Locate and identify every blood parasite.
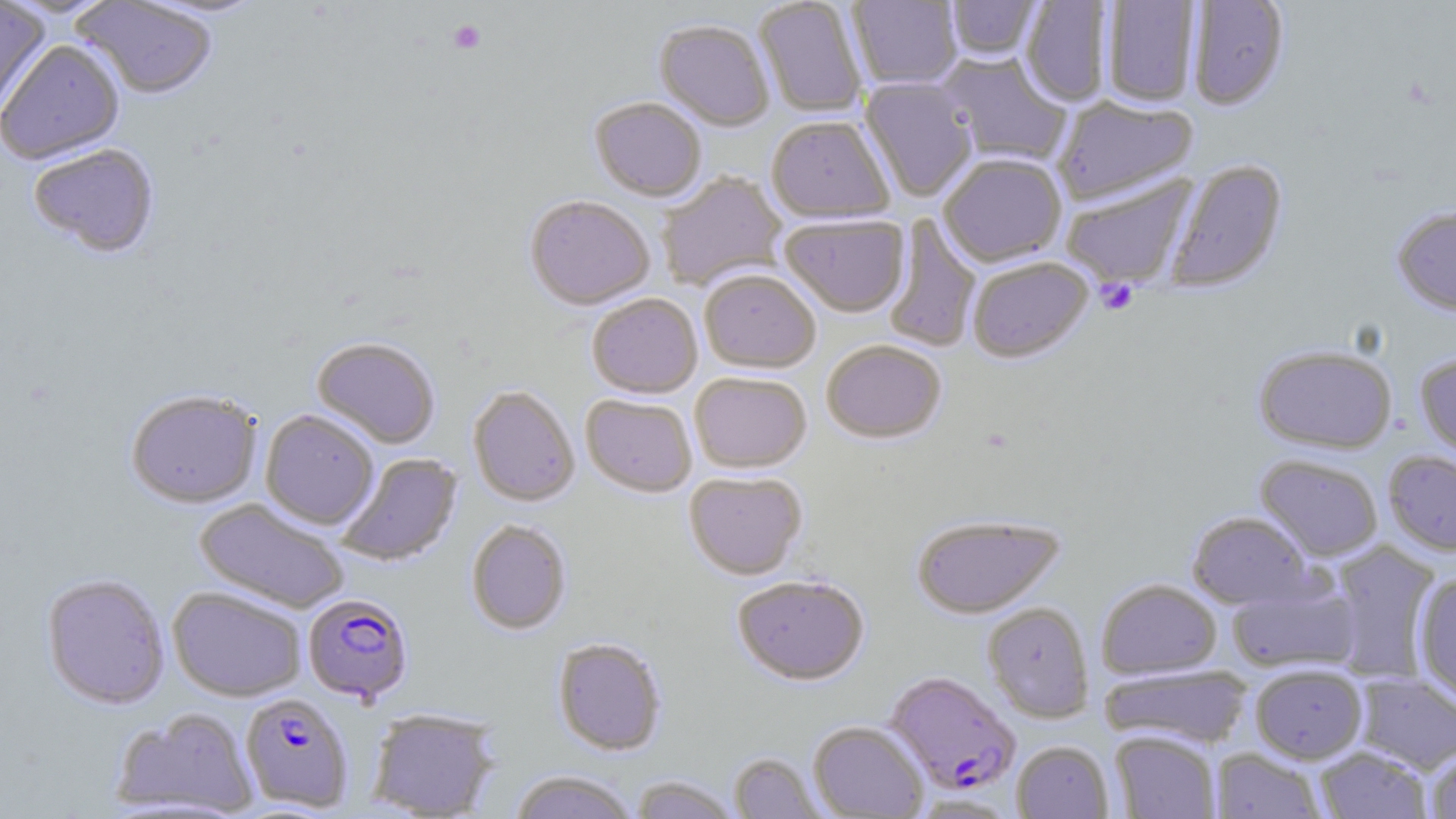

Approximate bounding boxes as (x1, y1, x2, y2) in pixels.
Plasmodium falciparum-infected red blood cells: (302, 593, 415, 704), (884, 670, 1021, 795), (240, 692, 354, 812).
No Plasmodium ovale, Plasmodium malariae, Plasmodium vivax, Babesia divergens, or Trypanosoma brucei observed.

{
  "slide_level_diagnosis": "Plasmodium falciparum",
  "image_size": "1456×819 pixels",
  "magnification": "1000x",
  "modality": "light microscopy",
  "uninfected_red_blood_cell_locations": "approximate bounding boxes as (x1, y1, x2, y2) in pixels: (753, 0, 868, 118), (847, 0, 962, 90), (1185, 0, 1290, 111), (0, 1, 51, 120), (71, 1, 218, 99), (945, 1, 1043, 63), (1020, 1, 1114, 107), (1101, 1, 1201, 106), (654, 20, 775, 131), (1, 40, 125, 165), (936, 52, 1072, 166), (859, 77, 978, 202), (1053, 95, 1198, 205), (590, 97, 706, 201), (766, 115, 895, 223), (27, 143, 159, 258), (938, 153, 1067, 267), (1165, 158, 1288, 294), (656, 172, 787, 291), (1060, 174, 1197, 289), (525, 194, 655, 310), (1391, 205, 1456, 316), (780, 214, 909, 317), (883, 216, 981, 354), (967, 255, 1093, 363), (699, 268, 821, 373), (587, 293, 702, 398), (312, 336, 440, 449), (323, 338, 448, 567), (821, 339, 946, 443), (1254, 344, 1397, 454), (1414, 352, 1456, 466), (689, 371, 812, 473), (467, 385, 580, 506), (125, 389, 262, 509), (581, 394, 697, 496), (260, 409, 379, 529), (1383, 450, 1456, 556), (336, 452, 462, 567), (1255, 454, 1383, 561), (684, 471, 808, 580), (195, 498, 350, 614), (1187, 511, 1313, 609), (911, 514, 1065, 619), (466, 520, 572, 635), (1327, 540, 1441, 683), (41, 573, 170, 710), (732, 573, 869, 685), (1413, 573, 1456, 706), (1096, 578, 1222, 680), (1228, 579, 1360, 675), (167, 586, 307, 702), (982, 602, 1094, 722), (553, 637, 667, 756), (1100, 664, 1253, 749), (1250, 664, 1368, 763), (1353, 673, 1456, 773), (112, 707, 258, 816), (368, 708, 500, 818), (808, 720, 928, 818), (1111, 730, 1221, 819), (1012, 741, 1113, 819), (1426, 745, 1456, 819), (1316, 746, 1432, 818), (1211, 748, 1326, 818), (729, 752, 827, 818), (508, 770, 639, 819), (630, 776, 741, 818), (907, 794, 1020, 818)",
  "stain": "May-Grünwald-Giemsa",
  "field_of_view": "one of a larger specimen",
  "platelet_locations": "approximate bounding boxes as (x1, y1, x2, y2) in pixels: (447, 19, 486, 54), (1095, 278, 1139, 315)",
  "preparation": "thin blood smear"
}